Classify this cell by malaria status.
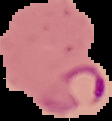
Parasitized.

Summary:
  - Image type: segmented cell region with the area outside set to black
  - Image size: 112×121 pixels
  - Preparation: thin blood film